Outline each uninfected red blood cell.
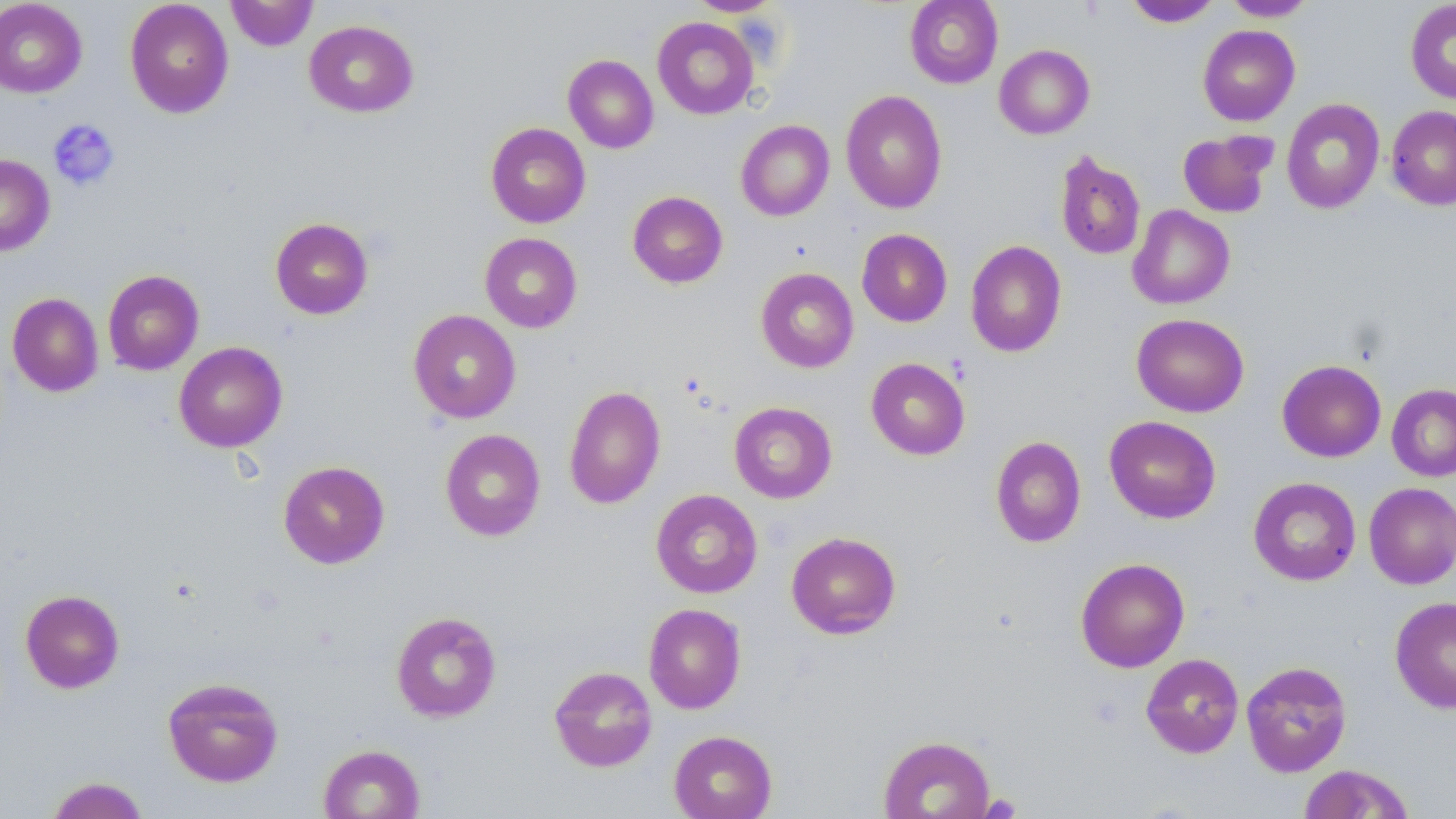
Approximate bounding boxes as (x1, y1, x2, y2) in pixels.
Uninfected red blood cells: (124, 0, 234, 118), (226, 0, 318, 51), (686, 0, 782, 16), (905, 0, 1003, 89), (1222, 0, 1317, 21), (1405, 0, 1456, 105), (0, 1, 88, 98), (1124, 1, 1222, 27), (652, 17, 759, 120), (304, 20, 418, 117), (1197, 24, 1300, 126), (994, 44, 1095, 140), (563, 54, 658, 153), (840, 89, 948, 214), (1281, 98, 1385, 214), (1386, 106, 1456, 209), (736, 120, 834, 221), (485, 122, 591, 228), (1178, 131, 1275, 218), (1055, 151, 1146, 261), (0, 154, 55, 255), (627, 191, 728, 288), (1127, 205, 1235, 309), (270, 217, 374, 320), (857, 228, 953, 327), (480, 232, 582, 333), (966, 240, 1067, 357), (755, 267, 859, 373), (102, 269, 204, 375), (7, 292, 103, 397), (408, 309, 521, 424), (1131, 313, 1249, 417), (174, 341, 288, 452), (866, 357, 970, 460), (1277, 359, 1386, 462), (1387, 383, 1456, 481), (564, 385, 666, 509), (729, 402, 837, 503), (1104, 416, 1221, 524), (440, 429, 546, 541), (990, 436, 1086, 548), (278, 460, 390, 569), (1248, 477, 1361, 586), (1364, 482, 1456, 589), (651, 489, 763, 598), (786, 531, 901, 639), (1075, 557, 1190, 673), (20, 589, 125, 693), (1390, 595, 1456, 714), (643, 603, 746, 714), (391, 611, 502, 722), (1141, 653, 1244, 758), (1241, 660, 1352, 777), (549, 665, 657, 772), (162, 676, 284, 788), (668, 730, 777, 819), (878, 734, 996, 819), (318, 743, 425, 818), (1297, 763, 1416, 818), (45, 776, 150, 818).

slide_level_diagnosis: negative for blood parasites
magnification: 1000x
preparation: thin blood film
platelet_locations: 'approximate bounding boxes as (x1, y1, x2, y2) in pixels: (47, 118, 120, 190), (978, 793, 1022, 818)'
image_size: 1456×819 pixels
stain: May-Grünwald-Giemsa
field_of_view: single
modality: optical microscopy